Give the extent of all Plasmodium falciparum-infected red blood cells.
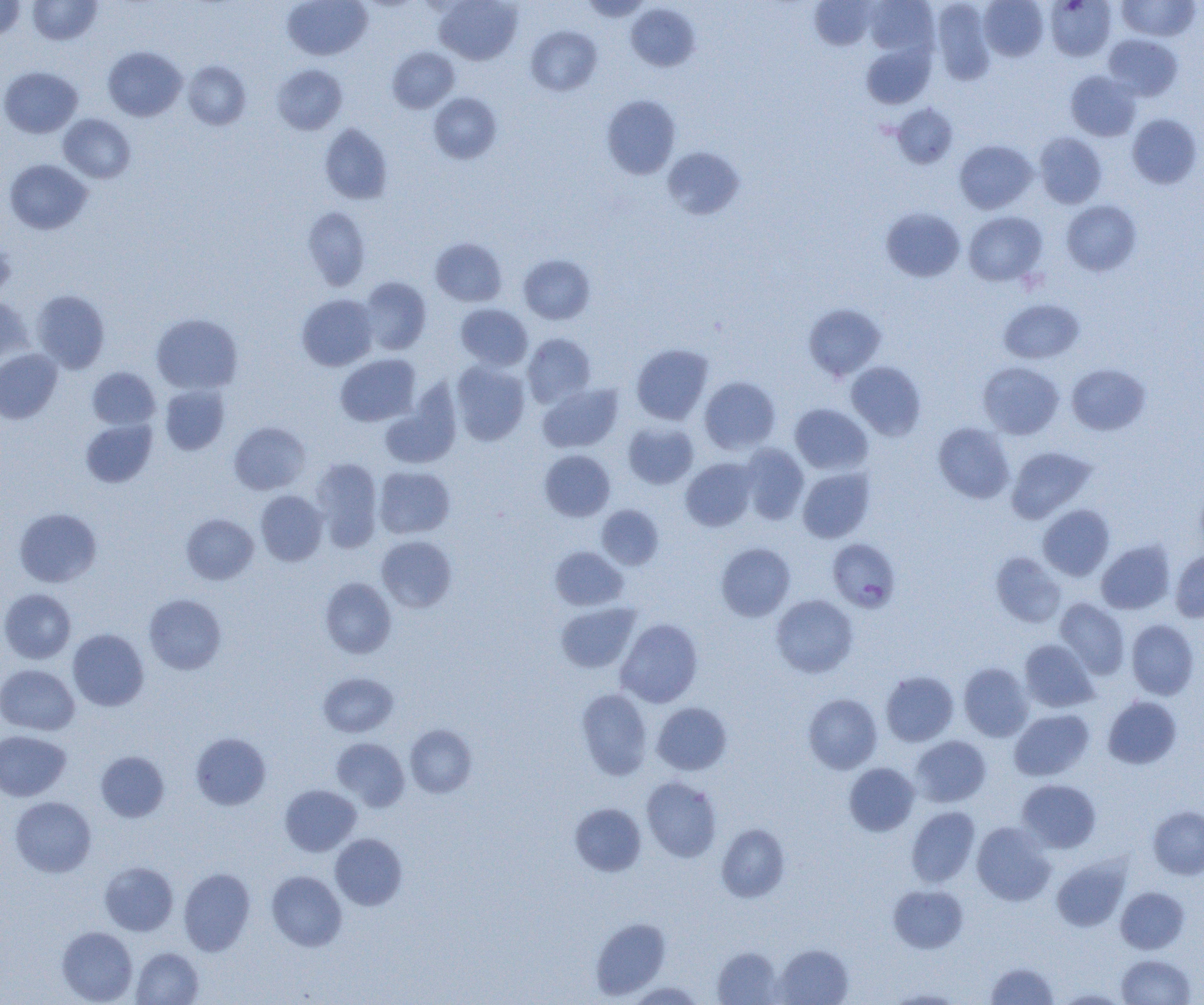
Approximate bounding boxes as [x1, y1, x2, y2] in pixels.
Plasmodium falciparum-infected red blood cells: [828, 541, 900, 614].

slide-level diagnosis = Plasmodium falciparum
modality = light microscopy
magnification = 1000x
uninfected red blood cell locations = approximate bounding boxes as [x1, y1, x2, y2] in pixels: [27, 0, 102, 45], [282, 0, 372, 60], [434, 0, 523, 65], [580, 0, 652, 21], [809, 0, 877, 50], [865, 0, 939, 57], [979, 0, 1048, 61], [1048, 0, 1119, 58], [1116, 0, 1199, 41], [0, 1, 25, 40], [931, 1, 996, 85], [626, 4, 699, 71], [526, 26, 602, 95], [1103, 34, 1182, 101], [861, 43, 935, 108], [103, 46, 186, 121], [387, 47, 459, 113], [183, 61, 251, 130], [272, 64, 348, 135], [0, 66, 82, 137], [1065, 70, 1141, 141], [429, 93, 501, 164], [601, 95, 681, 179], [892, 104, 958, 168], [58, 113, 136, 183], [1127, 113, 1202, 188], [319, 124, 393, 205], [1034, 132, 1107, 208], [955, 140, 1037, 214], [662, 147, 744, 219], [4, 159, 92, 235], [1061, 200, 1141, 276], [302, 206, 370, 291], [881, 207, 966, 282], [964, 211, 1047, 286], [430, 238, 507, 306], [0, 241, 15, 295], [519, 254, 595, 324], [358, 276, 431, 355], [31, 290, 110, 373], [297, 294, 378, 370], [0, 296, 32, 367], [999, 299, 1084, 364], [803, 303, 886, 381], [455, 304, 532, 370], [151, 314, 243, 394], [523, 333, 596, 408], [631, 344, 713, 425], [0, 348, 62, 423], [335, 354, 420, 426], [451, 361, 530, 445], [846, 361, 926, 440], [978, 361, 1064, 439], [1066, 364, 1150, 435], [87, 366, 160, 430], [699, 376, 781, 454], [537, 383, 623, 452], [160, 385, 230, 454], [381, 386, 460, 470], [790, 404, 872, 475], [80, 419, 157, 488], [229, 421, 311, 495], [623, 422, 699, 489], [933, 422, 1014, 504], [738, 444, 809, 525], [1006, 446, 1095, 523], [539, 450, 615, 521], [310, 458, 383, 552], [681, 458, 758, 531], [375, 466, 455, 539], [798, 467, 874, 543], [256, 490, 328, 566], [1038, 504, 1114, 581], [596, 505, 664, 570], [15, 508, 101, 587], [181, 514, 259, 585], [377, 535, 457, 612], [1096, 540, 1175, 614], [716, 543, 795, 621], [550, 546, 628, 610], [1170, 550, 1204, 622], [991, 552, 1066, 628], [320, 577, 396, 658], [0, 588, 76, 664], [144, 593, 227, 674], [771, 594, 858, 677], [1055, 598, 1129, 679], [556, 602, 640, 673], [616, 618, 703, 707], [1126, 619, 1199, 700], [68, 629, 149, 710], [1019, 639, 1098, 712], [959, 662, 1033, 742], [0, 664, 79, 735], [881, 670, 958, 746], [319, 672, 398, 737], [576, 688, 652, 780], [803, 693, 882, 774], [1102, 696, 1181, 769], [652, 702, 732, 775], [1010, 709, 1093, 780], [405, 724, 478, 798], [0, 730, 70, 801], [191, 732, 271, 809], [910, 735, 990, 807], [331, 738, 410, 811], [96, 751, 169, 822], [844, 762, 919, 836], [642, 776, 722, 862], [1017, 779, 1101, 852], [280, 784, 361, 856], [10, 796, 96, 877], [570, 803, 646, 876], [906, 806, 980, 887], [1148, 806, 1204, 879], [972, 822, 1055, 906], [716, 824, 790, 903], [330, 833, 407, 910], [1051, 857, 1130, 931], [99, 861, 178, 936], [179, 868, 255, 956], [266, 870, 347, 951], [888, 884, 968, 953], [1116, 886, 1190, 953], [590, 917, 670, 1000], [56, 926, 138, 1004], [774, 944, 853, 1004], [712, 946, 784, 1004], [132, 947, 204, 1005], [1116, 954, 1196, 1004], [986, 961, 1058, 1004], [625, 981, 705, 1004], [886, 989, 965, 1004], [1054, 989, 1130, 1004]
image size = 1204×1005 pixels
field of view = one of a larger specimen
preparation = thin blood film